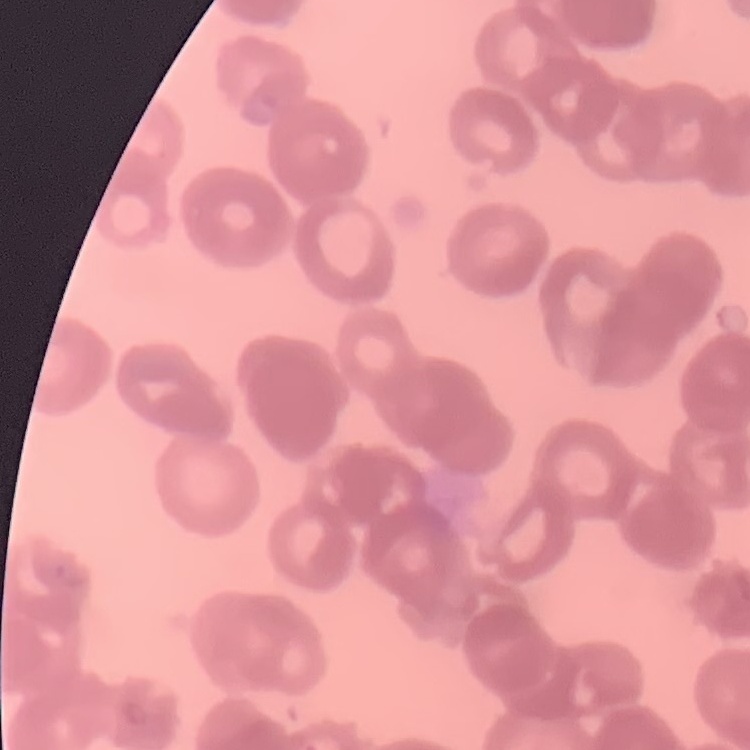
erythrocyte_morphology: rouleaux formation
preparation: thin blood film
stain: Field's or Giemsa
image_type: square crop of a larger photomicrograph